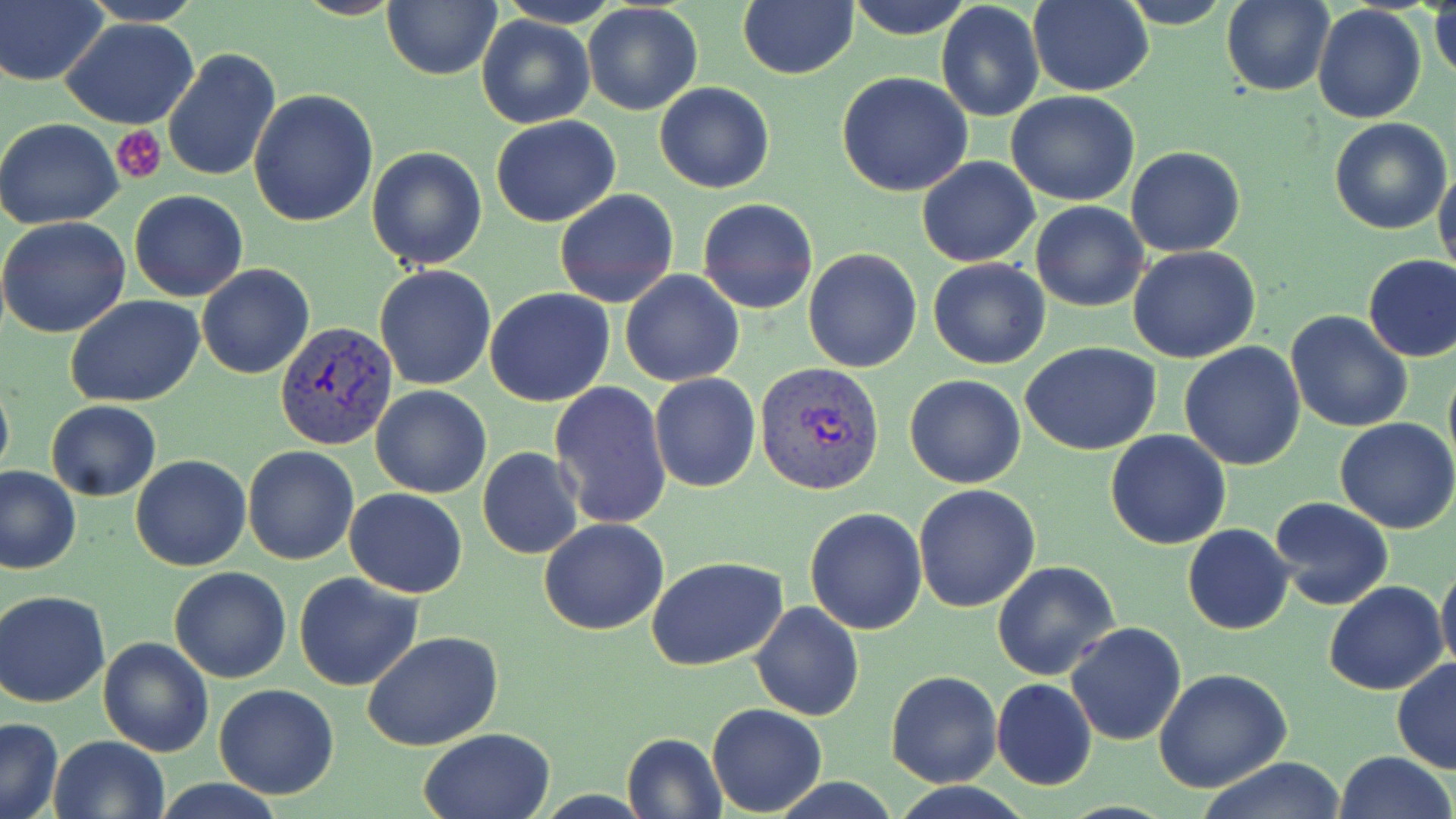

slide_level_diagnosis: Plasmodium vivax
magnification: 1000x
image_size: 1456×819 pixels
modality: light microscopy
uninfected_red_blood_cell_locations: 'approximate bounding boxes as (x1, y1, x2, y2) in pixels: (495, 0, 625, 28), (736, 0, 857, 80), (844, 0, 974, 38), (1027, 0, 1153, 96), (1114, 0, 1234, 29), (1, 1, 107, 86), (81, 1, 204, 25), (382, 1, 501, 80), (1222, 1, 1335, 97), (1430, 1, 1456, 82), (935, 2, 1044, 121), (582, 3, 703, 116), (1313, 5, 1427, 125), (477, 14, 594, 128), (62, 18, 200, 129), (161, 48, 281, 183), (837, 71, 974, 195), (654, 81, 775, 194), (248, 89, 379, 229), (1005, 91, 1140, 207), (490, 116, 621, 227), (0, 118, 124, 230), (1329, 118, 1452, 235), (366, 145, 489, 269), (1125, 146, 1247, 257), (916, 157, 1040, 268), (1433, 162, 1456, 281), (554, 188, 679, 309), (129, 190, 249, 302), (697, 198, 818, 315), (1029, 201, 1149, 313), (0, 216, 132, 338), (1128, 246, 1261, 365), (803, 248, 921, 373), (1362, 253, 1456, 363), (928, 258, 1051, 369), (197, 264, 314, 379), (373, 264, 497, 391), (619, 270, 744, 388), (484, 288, 616, 407), (66, 295, 206, 406), (1284, 308, 1413, 434), (1179, 341, 1306, 470), (1021, 342, 1164, 456), (1443, 356, 1456, 478), (648, 374, 760, 492), (904, 374, 1027, 489), (0, 376, 14, 483), (549, 381, 672, 531), (370, 385, 491, 498), (47, 401, 161, 501), (1334, 417, 1456, 534), (1105, 431, 1233, 549), (242, 447, 360, 565), (477, 447, 583, 560), (130, 455, 252, 571), (0, 466, 81, 577), (912, 484, 1041, 613), (345, 488, 468, 598), (1268, 496, 1395, 610), (805, 507, 928, 633), (538, 518, 669, 636), (1183, 524, 1295, 635), (646, 556, 789, 672), (1436, 559, 1456, 678), (992, 561, 1121, 682), (168, 566, 291, 682), (294, 572, 424, 693), (1323, 581, 1448, 696), (0, 589, 111, 708), (750, 601, 865, 720), (1065, 622, 1187, 747), (362, 632, 503, 752), (97, 636, 214, 756), (1391, 656, 1456, 775), (1154, 669, 1294, 792), (885, 671, 1001, 788), (990, 679, 1096, 791), (213, 684, 340, 799), (707, 703, 827, 816), (0, 717, 64, 819), (417, 728, 555, 818), (621, 731, 726, 818), (47, 735, 171, 819), (1333, 750, 1455, 819), (1196, 758, 1348, 819), (888, 783, 1035, 818)'
preparation: thin blood film
platelet_locations: 'approximate bounding boxes as (x1, y1, x2, y2) in pixels: (113, 127, 169, 183)'
plasmodium_vivax_infected_red_blood_cell_locations: 'approximate bounding boxes as (x1, y1, x2, y2) in pixels: (274, 320, 398, 449), (755, 363, 885, 496)'
field_of_view: single
stain: May-Grünwald-Giemsa